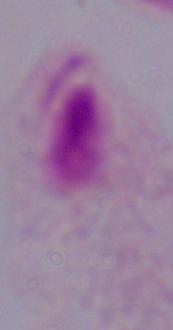
Summary:
  - Modality: photomicrograph
  - Identification: trichomonad
  - Magnification: 1000x